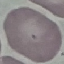

Summary:
  - Malaria status: uninfected
  - Capture: smartphone through the microscope eyepiece
  - Stain: Giemsa
  - Preparation: thin smear
  - Image type: cell patch, automatically extracted from a larger field of view and resized to 64 × 64 pixels